State which parasite is depicted.
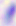

Toxoplasma gondii.

modality: photomicrograph
magnification: 400x